Classify this cell by malaria status.
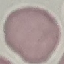

It is uninfected.

Summary:
  - Capture: smartphone camera at the microscope eyepiece
  - Preparation: thin blood smear
  - Stain: Giemsa
  - Image type: automatically extracted cell patch, resized to 64 × 64 pixels